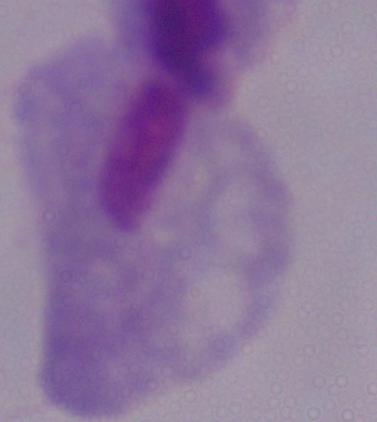
Captured at 1000x magnification. A trichomonad is shown. Photomicrograph.